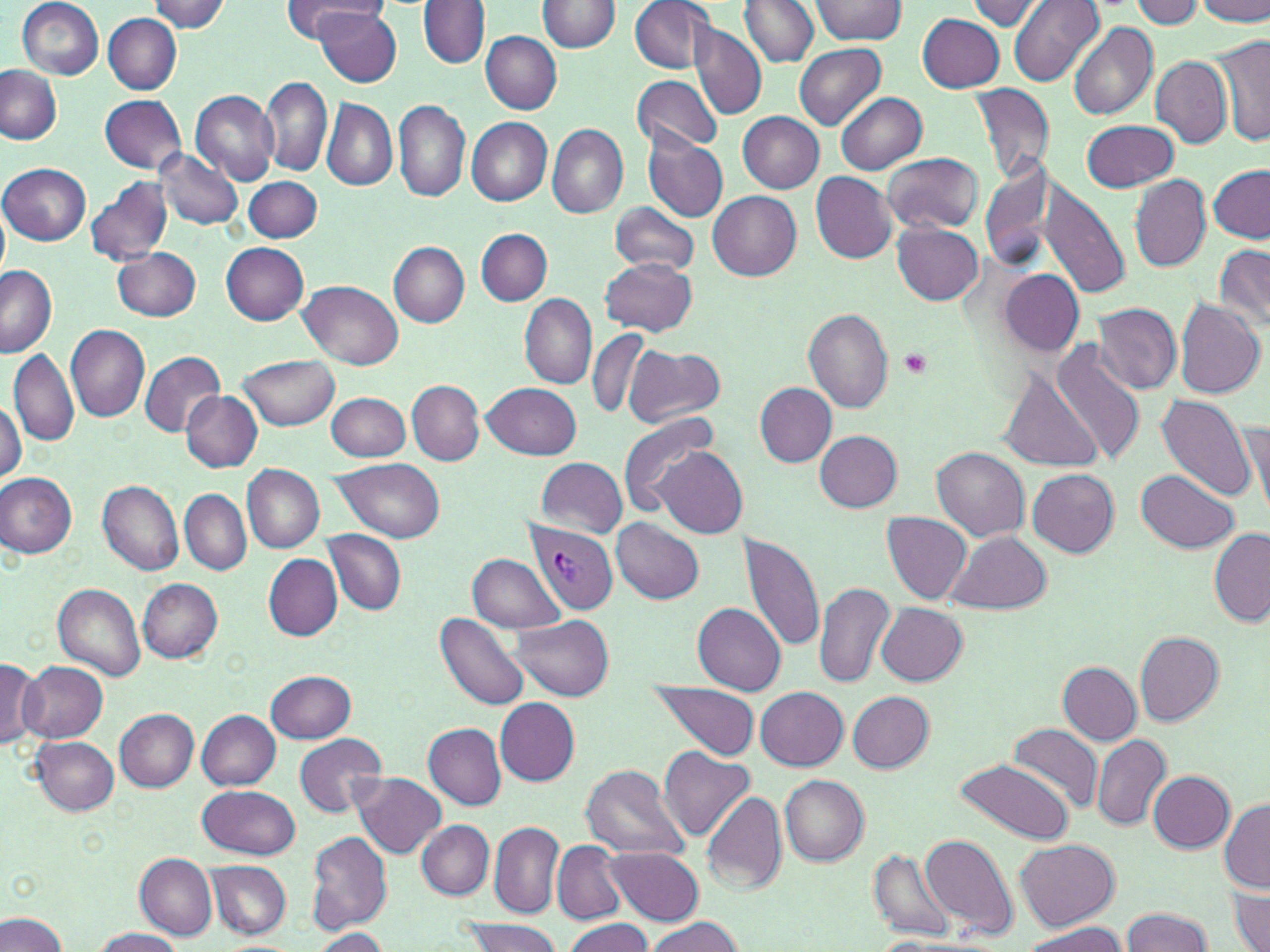
slide_level_diagnosis: Plasmodium vivax
magnification: 1000x
uninfected_red_blood_cell_locations: 'approximate bounding boxes as (x1, y1, x2, y2) in pixels: (18, 0, 105, 79), (281, 0, 384, 41), (629, 0, 714, 74), (741, 0, 819, 66), (813, 0, 907, 44), (1010, 0, 1105, 88), (1130, 0, 1204, 29), (1197, 0, 1270, 25), (152, 1, 231, 33), (418, 1, 489, 69), (537, 1, 621, 54), (965, 1, 1047, 31), (314, 5, 402, 87), (104, 13, 182, 94), (917, 13, 1005, 93), (689, 20, 767, 121), (1068, 23, 1158, 120), (479, 31, 562, 114), (1213, 35, 1270, 148), (794, 42, 886, 129), (1151, 56, 1232, 148), (0, 65, 62, 145), (630, 73, 724, 156), (260, 74, 332, 177), (969, 83, 1056, 186), (190, 89, 279, 185), (836, 92, 927, 175), (100, 95, 188, 174), (322, 98, 398, 192), (394, 100, 470, 202), (739, 112, 825, 193), (467, 117, 552, 205), (1082, 120, 1179, 192), (547, 123, 627, 218), (644, 136, 728, 221), (154, 149, 243, 231), (881, 153, 984, 234), (976, 161, 1061, 271), (0, 163, 90, 245), (1207, 165, 1270, 243), (811, 172, 896, 263), (1130, 173, 1210, 272), (85, 175, 173, 268), (245, 177, 323, 243), (1040, 183, 1132, 299), (707, 190, 802, 279), (610, 202, 700, 274), (0, 206, 9, 280), (892, 223, 984, 305), (476, 228, 551, 305), (221, 241, 309, 324), (390, 244, 469, 327), (1215, 245, 1270, 331), (114, 248, 201, 321), (599, 256, 697, 336), (0, 264, 57, 358), (997, 267, 1084, 357), (299, 281, 402, 370), (521, 293, 597, 388), (1175, 301, 1265, 400), (1093, 302, 1181, 394), (803, 308, 893, 414), (65, 324, 150, 422), (587, 329, 651, 418), (1051, 341, 1146, 466), (625, 345, 725, 426), (8, 349, 79, 447), (139, 350, 225, 436), (237, 354, 340, 431), (1000, 372, 1103, 471), (408, 381, 483, 464), (484, 381, 580, 459), (756, 383, 837, 466), (181, 391, 262, 471), (328, 392, 410, 462), (1158, 396, 1258, 503), (0, 399, 26, 483), (616, 410, 720, 519), (1243, 415, 1270, 515), (816, 432, 903, 511), (655, 446, 747, 538), (932, 447, 1029, 542), (536, 456, 628, 537), (333, 458, 446, 541), (242, 465, 325, 553), (1028, 469, 1118, 556), (1136, 469, 1239, 553), (0, 473, 78, 558), (97, 478, 183, 576), (182, 490, 252, 575), (882, 512, 973, 605), (611, 518, 704, 604), (1211, 528, 1270, 627), (324, 531, 406, 615), (949, 532, 1051, 615), (740, 534, 825, 651), (468, 552, 567, 635), (264, 555, 341, 640), (137, 578, 223, 662), (53, 580, 146, 682), (814, 580, 895, 688), (693, 601, 785, 693), (876, 603, 968, 685), (437, 612, 531, 711), (513, 614, 613, 699), (1135, 630, 1224, 725), (1, 660, 40, 749), (15, 660, 108, 743), (1059, 662, 1142, 744), (266, 669, 356, 743), (645, 682, 761, 761), (755, 687, 848, 771), (848, 692, 933, 771), (496, 698, 579, 784), (114, 708, 199, 790), (197, 710, 281, 789), (424, 723, 506, 810), (1007, 723, 1103, 813), (294, 732, 386, 816), (1092, 735, 1170, 831), (30, 736, 119, 814), (660, 746, 754, 843), (954, 757, 1075, 844), (581, 764, 692, 863), (1148, 771, 1233, 852), (353, 773, 446, 857), (779, 775, 869, 865), (198, 785, 299, 859), (700, 790, 788, 895), (1220, 800, 1269, 893), (417, 821, 494, 899), (489, 821, 565, 917), (307, 829, 393, 932), (919, 833, 1017, 941), (1015, 839, 1120, 930), (552, 840, 626, 924), (605, 848, 702, 924), (868, 849, 957, 942), (135, 853, 217, 940), (206, 861, 291, 940), (1230, 884, 1269, 952), (1121, 907, 1212, 952), (0, 912, 68, 952), (642, 918, 743, 952), (563, 919, 656, 952), (464, 920, 562, 952), (1020, 925, 1127, 952), (91, 927, 184, 952), (310, 929, 389, 950)'
image_size: 1270×952 pixels
preparation: thin blood smear
field_of_view: one of a larger specimen
platelet_locations: 'approximate bounding boxes as (x1, y1, x2, y2) in pixels: (901, 347, 934, 378)'
stain: May-Grünwald-Giemsa
modality: light microscopy
plasmodium_vivax_infected_red_blood_cell_locations: 'approximate bounding boxes as (x1, y1, x2, y2) in pixels: (525, 521, 619, 613)'